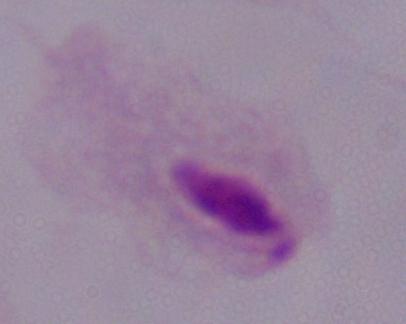
{
  "magnification": "1000x",
  "modality": "photomicrograph",
  "identification": "trichomonad"
}